Report the malaria status of this cell.
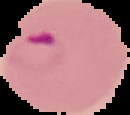
It is parasitized.

Summary:
  - Preparation: thin blood film
  - Image type: segmented cell region with the area outside set to black
  - Image size: 130×115 pixels